Comment on the morphology of the erythrocytes.
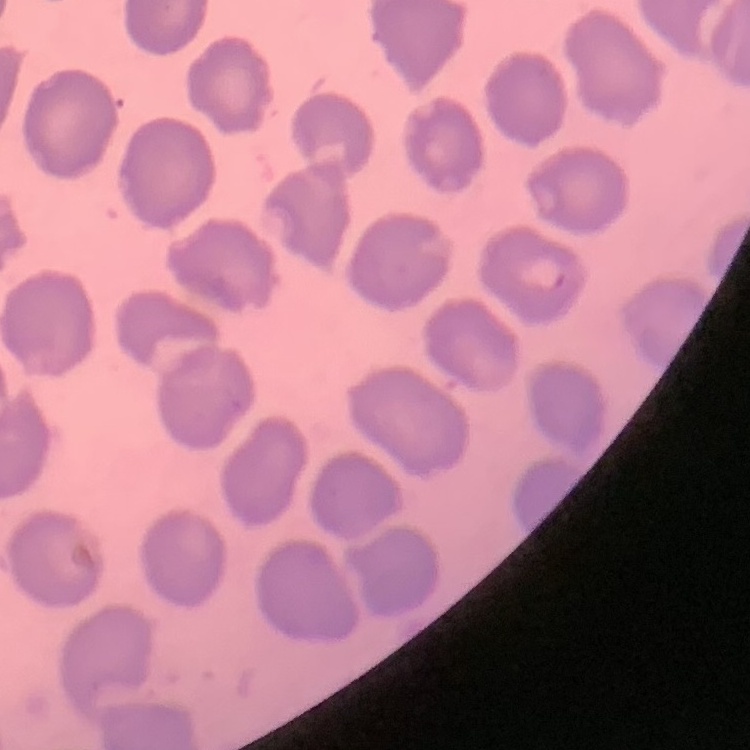
No rouleaux formation.

Summary:
  - Preparation: thin blood smear
  - Image type: one tile cut from a larger photomicrograph
  - Stain: Field's or Giemsa